Locate and identify every blood parasite.
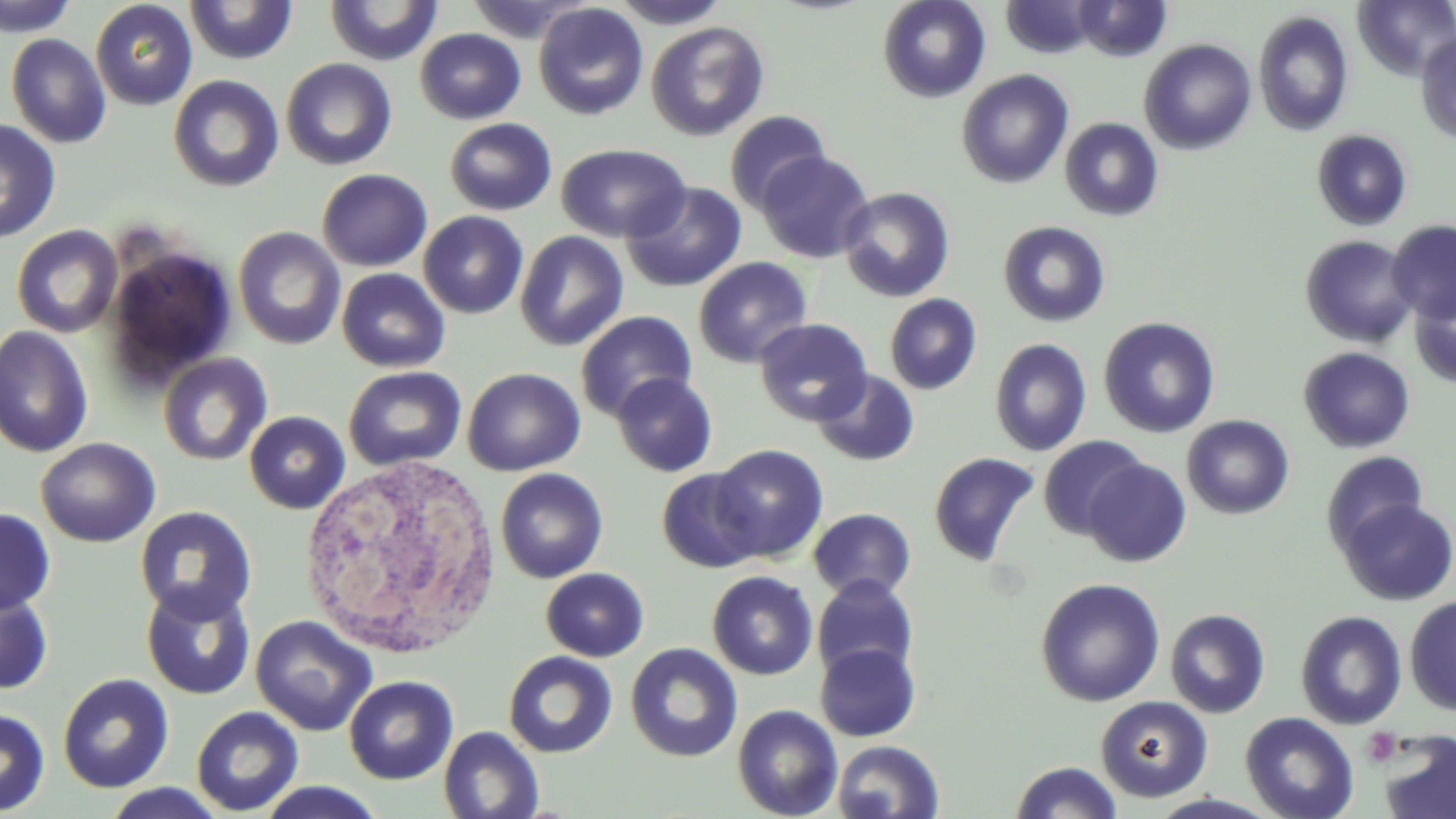

No blood parasites seen.

slide_level_diagnosis: no evidence of blood parasites
field_of_view: one of a larger specimen
modality: light microscopy
platelet_locations: 'approximate bounding boxes as named x1/y1/x2/y2 corners in pixels: (x1=1361, y1=728, x2=1402, y2=767)'
image_size: 1456×819 pixels
magnification: 1000x
stain: May-Grünwald-Giemsa
white_blood_cell_locations: 'approximate bounding boxes as named x1/y1/x2/y2 corners in pixels: (x1=297, y1=455, x2=503, y2=660)'
preparation: thin blood film
uninfected_red_blood_cell_locations: 'approximate bounding boxes as named x1/y1/x2/y2 corners in pixels: (x1=1, y1=0, x2=79, y2=37), (x1=609, y1=0, x2=732, y2=29), (x1=878, y1=0, x2=991, y2=103), (x1=1073, y1=0, x2=1172, y2=61), (x1=90, y1=1, x2=198, y2=110), (x1=184, y1=1, x2=298, y2=64), (x1=325, y1=1, x2=443, y2=65), (x1=463, y1=1, x2=591, y2=43), (x1=1001, y1=1, x2=1096, y2=58), (x1=1353, y1=1, x2=1456, y2=81), (x1=533, y1=2, x2=649, y2=120), (x1=1253, y1=10, x2=1354, y2=136), (x1=646, y1=21, x2=769, y2=141), (x1=415, y1=28, x2=526, y2=124), (x1=1415, y1=32, x2=1456, y2=143), (x1=6, y1=33, x2=112, y2=148), (x1=1139, y1=39, x2=1257, y2=154), (x1=281, y1=58, x2=397, y2=170), (x1=956, y1=69, x2=1074, y2=189), (x1=169, y1=75, x2=284, y2=192), (x1=724, y1=110, x2=831, y2=212), (x1=444, y1=117, x2=558, y2=215), (x1=1059, y1=117, x2=1164, y2=221), (x1=0, y1=120, x2=62, y2=243), (x1=1312, y1=130, x2=1412, y2=231), (x1=556, y1=143, x2=691, y2=242), (x1=756, y1=150, x2=875, y2=263), (x1=317, y1=168, x2=433, y2=271), (x1=621, y1=182, x2=748, y2=292), (x1=838, y1=187, x2=955, y2=303), (x1=418, y1=211, x2=528, y2=319), (x1=1387, y1=218, x2=1456, y2=323), (x1=997, y1=220, x2=1111, y2=327), (x1=11, y1=224, x2=123, y2=337), (x1=233, y1=226, x2=346, y2=349), (x1=514, y1=231, x2=629, y2=352), (x1=1300, y1=234, x2=1418, y2=347), (x1=104, y1=242, x2=236, y2=385), (x1=693, y1=257, x2=813, y2=368), (x1=337, y1=268, x2=451, y2=372), (x1=1409, y1=281, x2=1456, y2=388), (x1=885, y1=293, x2=982, y2=395), (x1=576, y1=310, x2=698, y2=421), (x1=1099, y1=316, x2=1221, y2=438), (x1=754, y1=317, x2=873, y2=426), (x1=0, y1=325, x2=94, y2=458), (x1=990, y1=338, x2=1092, y2=456), (x1=1298, y1=347, x2=1416, y2=453), (x1=158, y1=352, x2=273, y2=466), (x1=343, y1=365, x2=467, y2=471), (x1=462, y1=367, x2=585, y2=476), (x1=812, y1=369, x2=920, y2=467), (x1=611, y1=372, x2=718, y2=477), (x1=244, y1=411, x2=351, y2=513), (x1=1181, y1=414, x2=1295, y2=519), (x1=1038, y1=435, x2=1149, y2=540), (x1=35, y1=437, x2=161, y2=547), (x1=711, y1=444, x2=829, y2=562), (x1=1321, y1=450, x2=1429, y2=555), (x1=928, y1=451, x2=1040, y2=567), (x1=1082, y1=459, x2=1191, y2=567), (x1=495, y1=468, x2=608, y2=583), (x1=656, y1=469, x2=763, y2=573), (x1=1337, y1=498, x2=1456, y2=606), (x1=134, y1=506, x2=257, y2=624), (x1=0, y1=507, x2=56, y2=615), (x1=808, y1=508, x2=916, y2=601), (x1=541, y1=568, x2=649, y2=661), (x1=707, y1=570, x2=818, y2=680), (x1=812, y1=575, x2=919, y2=681), (x1=1035, y1=577, x2=1165, y2=707), (x1=0, y1=581, x2=55, y2=697), (x1=140, y1=582, x2=256, y2=700), (x1=1404, y1=594, x2=1456, y2=716), (x1=1164, y1=608, x2=1271, y2=718), (x1=1295, y1=611, x2=1408, y2=730), (x1=250, y1=615, x2=376, y2=736), (x1=625, y1=642, x2=743, y2=762), (x1=815, y1=642, x2=921, y2=741), (x1=504, y1=651, x2=617, y2=758), (x1=58, y1=673, x2=174, y2=793), (x1=344, y1=675, x2=458, y2=784), (x1=1095, y1=696, x2=1213, y2=802), (x1=732, y1=704, x2=843, y2=819), (x1=191, y1=706, x2=304, y2=816), (x1=0, y1=708, x2=50, y2=816), (x1=1239, y1=711, x2=1359, y2=819), (x1=439, y1=725, x2=544, y2=819), (x1=1378, y1=730, x2=1456, y2=819), (x1=832, y1=740, x2=945, y2=819), (x1=1010, y1=761, x2=1124, y2=819), (x1=255, y1=781, x2=386, y2=818), (x1=99, y1=783, x2=231, y2=818), (x1=1144, y1=793, x2=1287, y2=819)'